Identify the parasite.
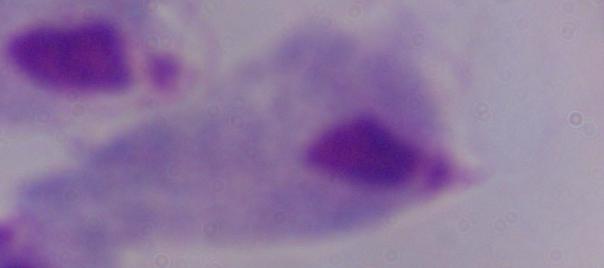
This is a trichomonad.

Summary:
  - Modality: photomicrograph
  - Magnification: 1000x